Describe the morphology of the red blood cells.
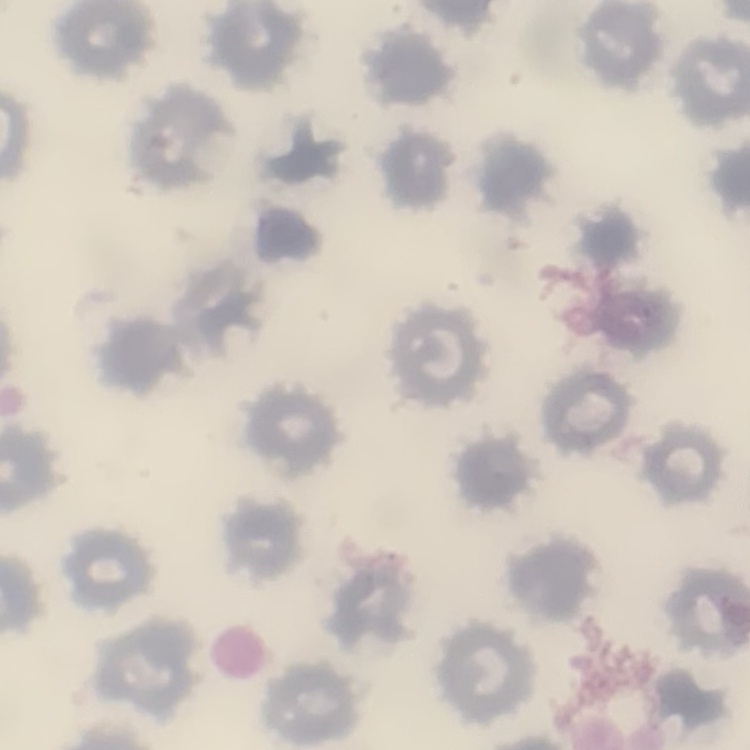

They show no rouleaux formation.

Summary:
  - Image type: square crop of a larger photomicrograph
  - Preparation: thin peripheral smear
  - Stain: Field's or Giemsa